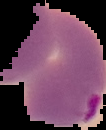
{
  "result": "malaria parasites identified",
  "image_type": "segmented cell region with the area outside set to black",
  "preparation": "thin blood film",
  "image_size": "106×130 pixels"
}